Identify the blood parasite species.
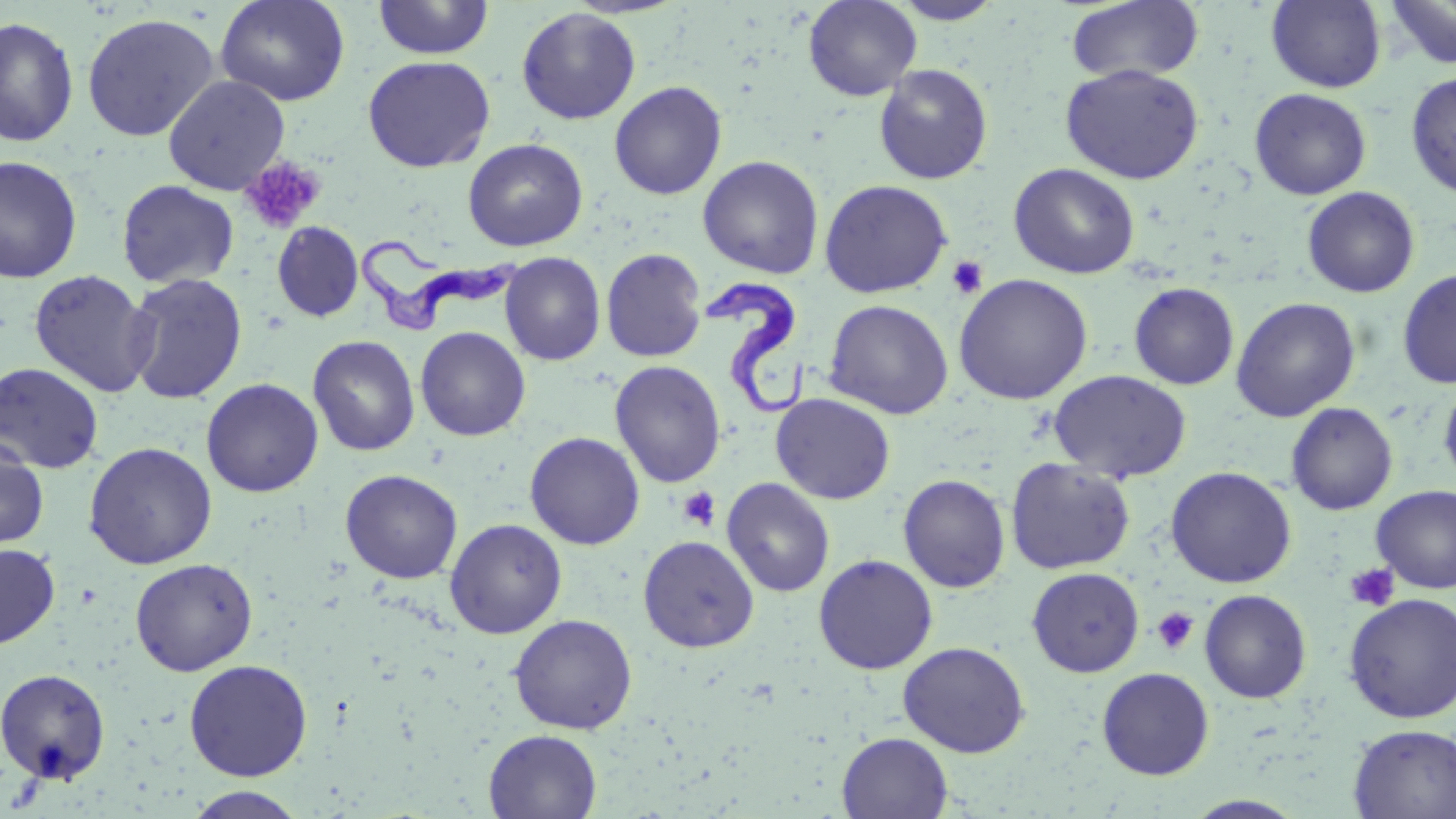
Trypanosoma brucei.

Summary:
  - Coordinate format: approximate bounding boxes as named x1/y1/x2/y2 corners in pixels
  - Trypanosoma brucei locations: (x1=356, y1=232, x2=516, y2=330), (x1=703, y1=279, x2=810, y2=414)
  - Uninfected red blood cell locations: (x1=215, y1=0, x2=350, y2=106), (x1=372, y1=0, x2=495, y2=60), (x1=802, y1=0, x2=922, y2=101), (x1=888, y1=0, x2=1006, y2=25), (x1=1266, y1=0, x2=1387, y2=93), (x1=1384, y1=0, x2=1456, y2=70), (x1=1066, y1=1, x2=1205, y2=85), (x1=516, y1=7, x2=641, y2=124), (x1=81, y1=12, x2=220, y2=142), (x1=0, y1=16, x2=79, y2=147), (x1=362, y1=55, x2=495, y2=172), (x1=1060, y1=62, x2=1205, y2=184), (x1=873, y1=64, x2=993, y2=185), (x1=1405, y1=72, x2=1456, y2=198), (x1=163, y1=75, x2=290, y2=195), (x1=609, y1=80, x2=727, y2=200), (x1=1249, y1=88, x2=1372, y2=200), (x1=463, y1=138, x2=588, y2=252), (x1=0, y1=155, x2=83, y2=284), (x1=698, y1=155, x2=824, y2=279), (x1=1008, y1=163, x2=1140, y2=279), (x1=117, y1=179, x2=239, y2=288), (x1=819, y1=179, x2=953, y2=298), (x1=1302, y1=186, x2=1420, y2=298), (x1=272, y1=222, x2=363, y2=322), (x1=601, y1=247, x2=708, y2=363), (x1=500, y1=252, x2=606, y2=366), (x1=29, y1=269, x2=157, y2=398), (x1=1397, y1=269, x2=1456, y2=389), (x1=124, y1=273, x2=248, y2=404), (x1=953, y1=273, x2=1093, y2=404), (x1=1128, y1=281, x2=1239, y2=390), (x1=1230, y1=297, x2=1360, y2=422), (x1=823, y1=299, x2=954, y2=419), (x1=415, y1=326, x2=530, y2=441), (x1=308, y1=335, x2=420, y2=456), (x1=609, y1=360, x2=726, y2=488), (x1=0, y1=362, x2=105, y2=474), (x1=1049, y1=369, x2=1192, y2=482), (x1=201, y1=378, x2=323, y2=497), (x1=1439, y1=380, x2=1456, y2=489), (x1=771, y1=393, x2=896, y2=505), (x1=1286, y1=402, x2=1398, y2=515), (x1=524, y1=431, x2=645, y2=550), (x1=0, y1=438, x2=49, y2=550), (x1=83, y1=441, x2=218, y2=569), (x1=1005, y1=457, x2=1136, y2=574), (x1=1165, y1=466, x2=1297, y2=588), (x1=340, y1=469, x2=463, y2=583), (x1=898, y1=474, x2=1010, y2=593), (x1=722, y1=478, x2=835, y2=597), (x1=1371, y1=485, x2=1456, y2=594), (x1=445, y1=518, x2=567, y2=638), (x1=638, y1=535, x2=759, y2=652), (x1=0, y1=543, x2=60, y2=649), (x1=813, y1=554, x2=939, y2=674), (x1=130, y1=558, x2=258, y2=675), (x1=1027, y1=567, x2=1145, y2=677), (x1=1199, y1=589, x2=1312, y2=703), (x1=1343, y1=592, x2=1456, y2=724), (x1=509, y1=614, x2=637, y2=734), (x1=897, y1=641, x2=1030, y2=757), (x1=184, y1=659, x2=313, y2=781), (x1=0, y1=667, x2=111, y2=784), (x1=1097, y1=667, x2=1214, y2=780), (x1=1348, y1=723, x2=1456, y2=818), (x1=483, y1=729, x2=602, y2=818), (x1=837, y1=732, x2=953, y2=818), (x1=184, y1=787, x2=309, y2=819), (x1=1184, y1=795, x2=1308, y2=818)
  - Platelet locations: (x1=239, y1=155, x2=325, y2=234), (x1=946, y1=255, x2=988, y2=299), (x1=678, y1=487, x2=721, y2=532), (x1=1344, y1=562, x2=1400, y2=611), (x1=1151, y1=606, x2=1199, y2=656)
  - Stain: May-Grünwald-Giemsa
  - Field of view: single
  - Magnification: 1000x
  - Preparation: thin blood film
  - Modality: light microscopy
  - Image size: 1456×819 pixels